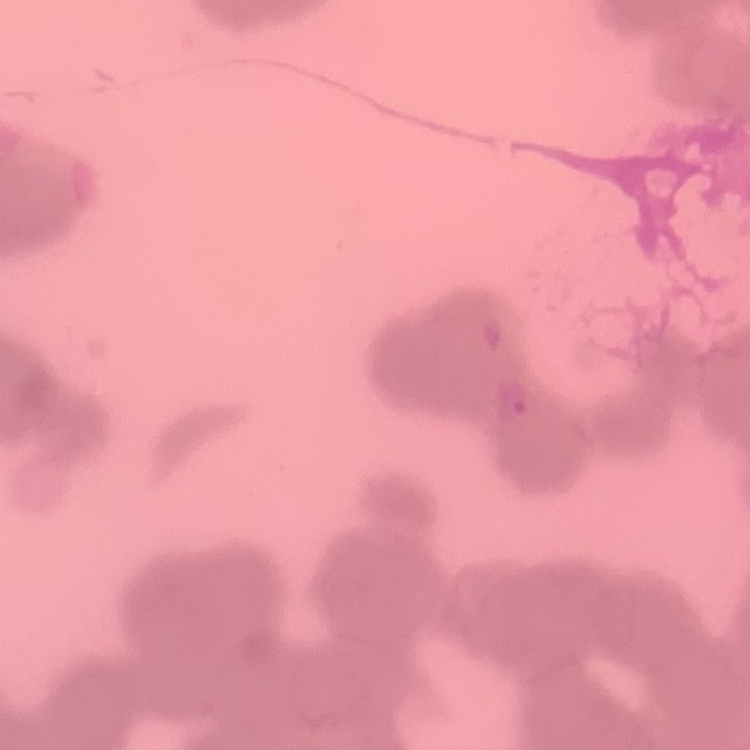

erythrocyte morphology = rouleaux formation
stain = Field's or Giemsa
preparation = thin peripheral smear
image type = square crop of a larger photomicrograph